Identify the parasite.
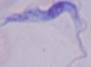

A trypanosome.

modality: photomicrograph
magnification: 1000x